Report the malaria status of this cell.
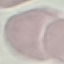
It is uninfected.

Summary:
  - Image type: cell patch, automatically extracted from a larger field of view and resized to 64 × 64 pixels
  - Preparation: thin blood smear
  - Stain: Giemsa
  - Capture: smartphone through the microscope eyepiece